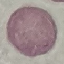

malaria status = uninfected
preparation = thin blood smear
image type = automatically extracted cell patch, resized to 64 × 64 pixels
stain = Giemsa
capture = smartphone through the microscope eyepiece